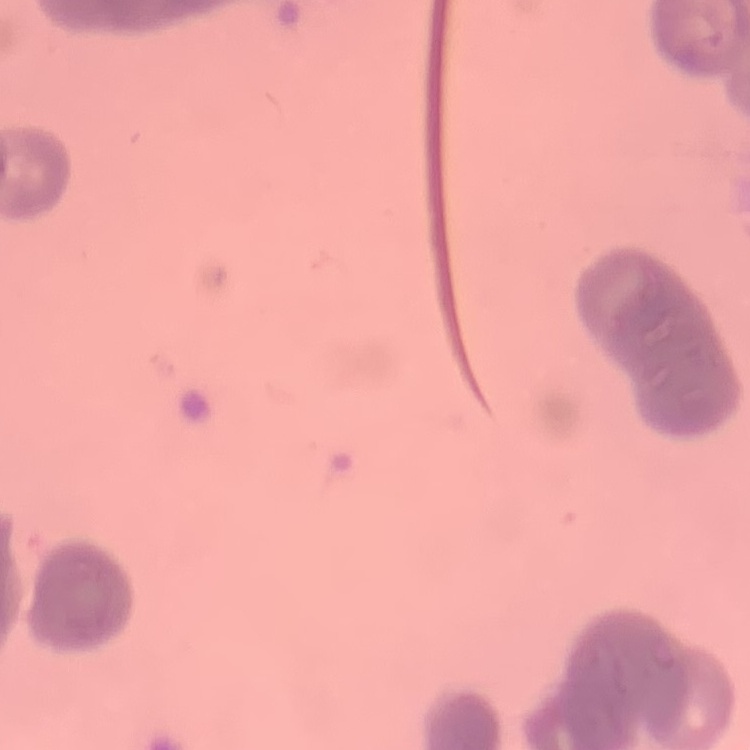

Summary:
  - Erythrocyte morphology: rouleaux formation
  - Preparation: thin blood smear
  - Stain: Field's or Giemsa
  - Image type: one tile cut from a larger photomicrograph